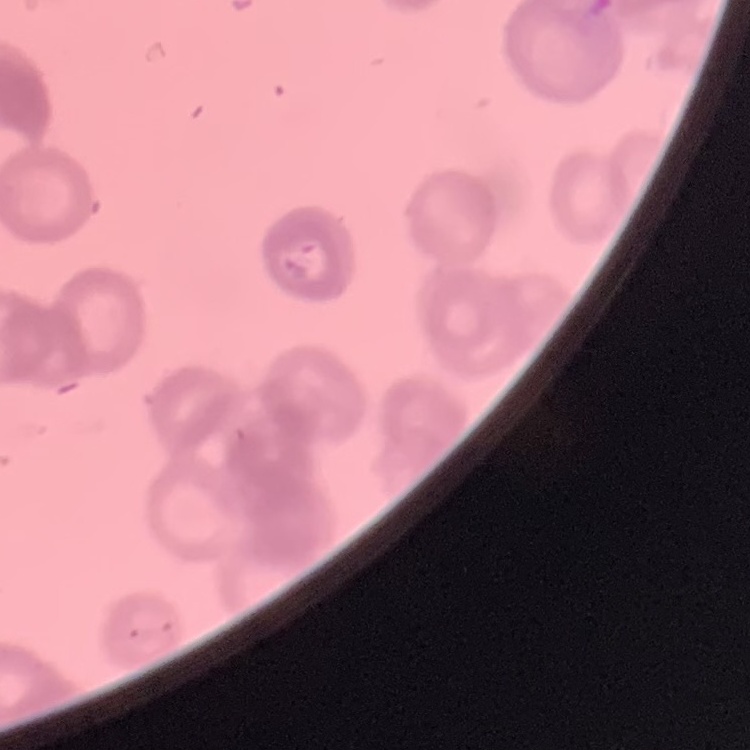
The erythrocytes show rouleaux formation. Field's or Giemsa stain. One tile cut from a larger photomicrograph. Thin blood smear.